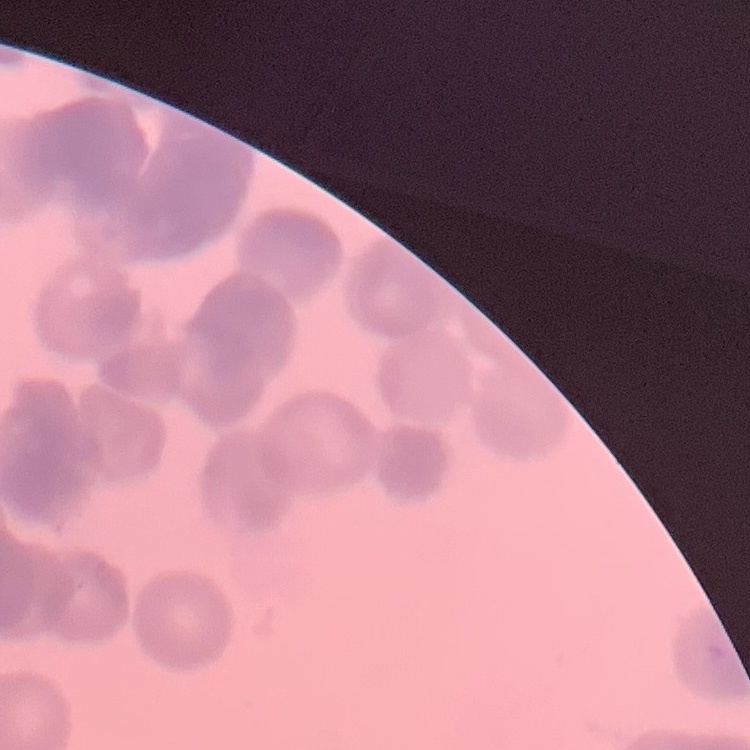

The red blood cells exhibit rouleaux formation. Stained with either Field's or Giemsa. Thin blood film. One tile cut from a larger photomicrograph.